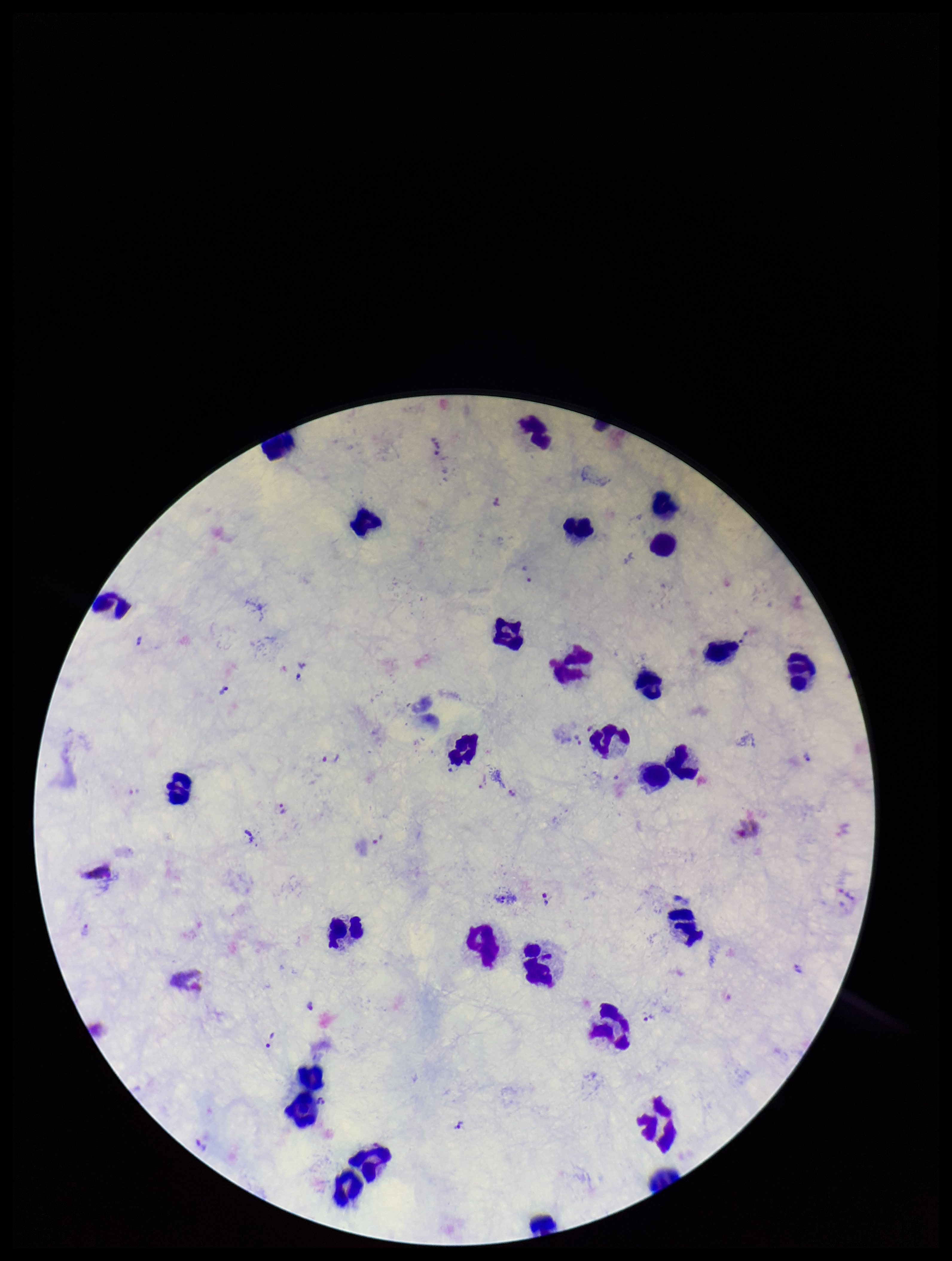 Species reported for this patient: Plasmodium vivax. Photographed through the microscope eyepiece with a smartphone camera. Patient malaria status: positive. Giemsa stain. Plasmodium parasites: seen. Preparation: thick. One field from this slide. Parasite count: 24. Leukocyte count: 25. Image is 952×1261 pixels.